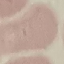
result: no malaria parasites detected
stain: Giemsa
capture: smartphone through the microscope eyepiece
image_type: cell patch, automatically extracted from a larger field of view and resized to 64 × 64 pixels
preparation: thin blood film